Locate every Plasmodium parasite.
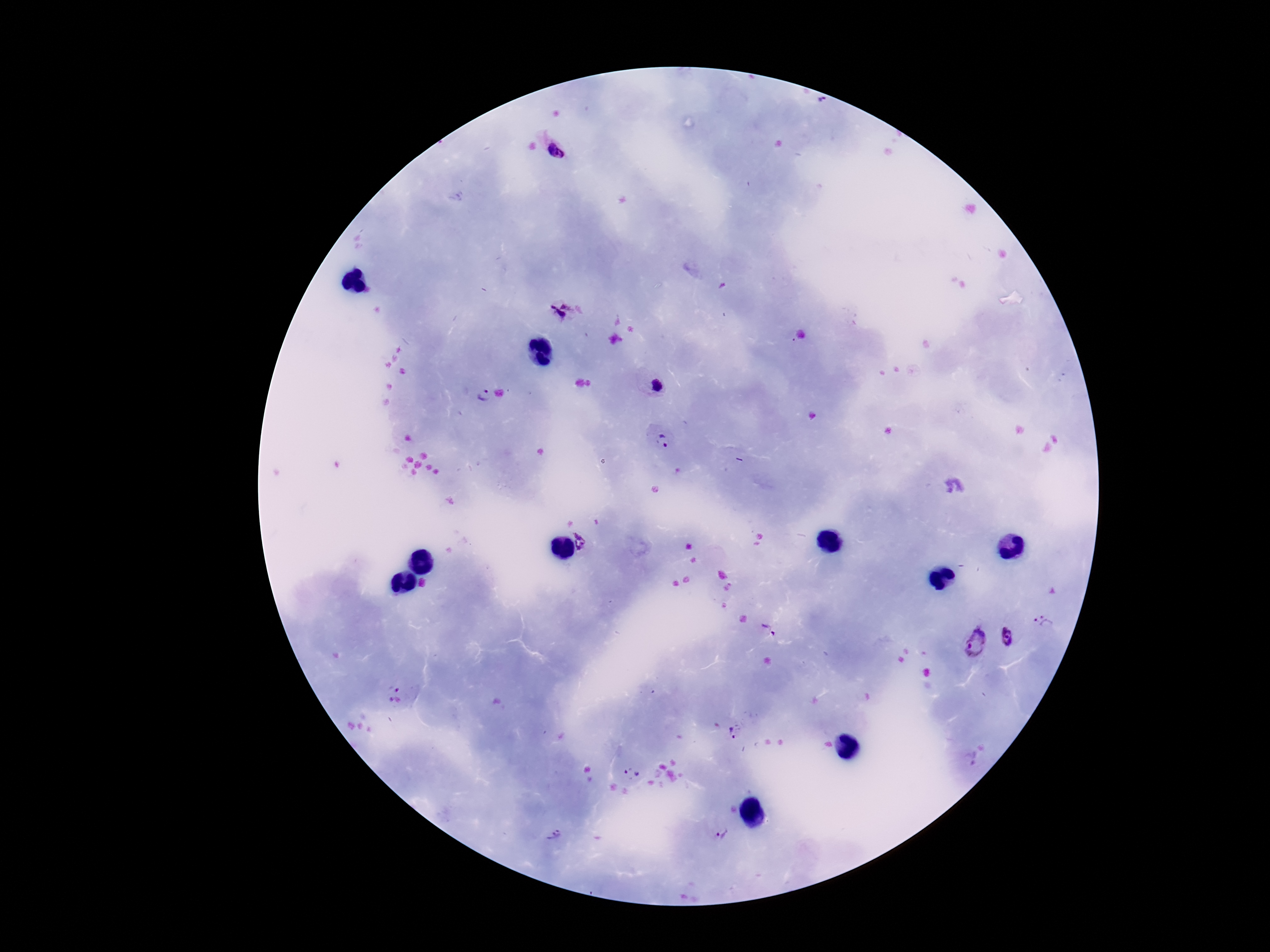

Approximate centers as {x, y} in pixels.
Plasmodium parasites: {554, 152}, {558, 310}, {655, 385}, {482, 395}, {663, 441}, {585, 541}, {1045, 622}, {769, 629}, {1008, 638}, {975, 643}, {396, 694}, {736, 731}, {632, 771}, {553, 835}, {722, 835}.

magnification: 100x
image_size: 1270×952 pixels
stain: Giemsa
patient_malaria_status: infected
capture: smartphone camera through the microscope eyepiece
field_of_view: one from this slide
preparation: thick peripheral-blood smear